Give the position of every Plasmodium parasite and every leukocyte.
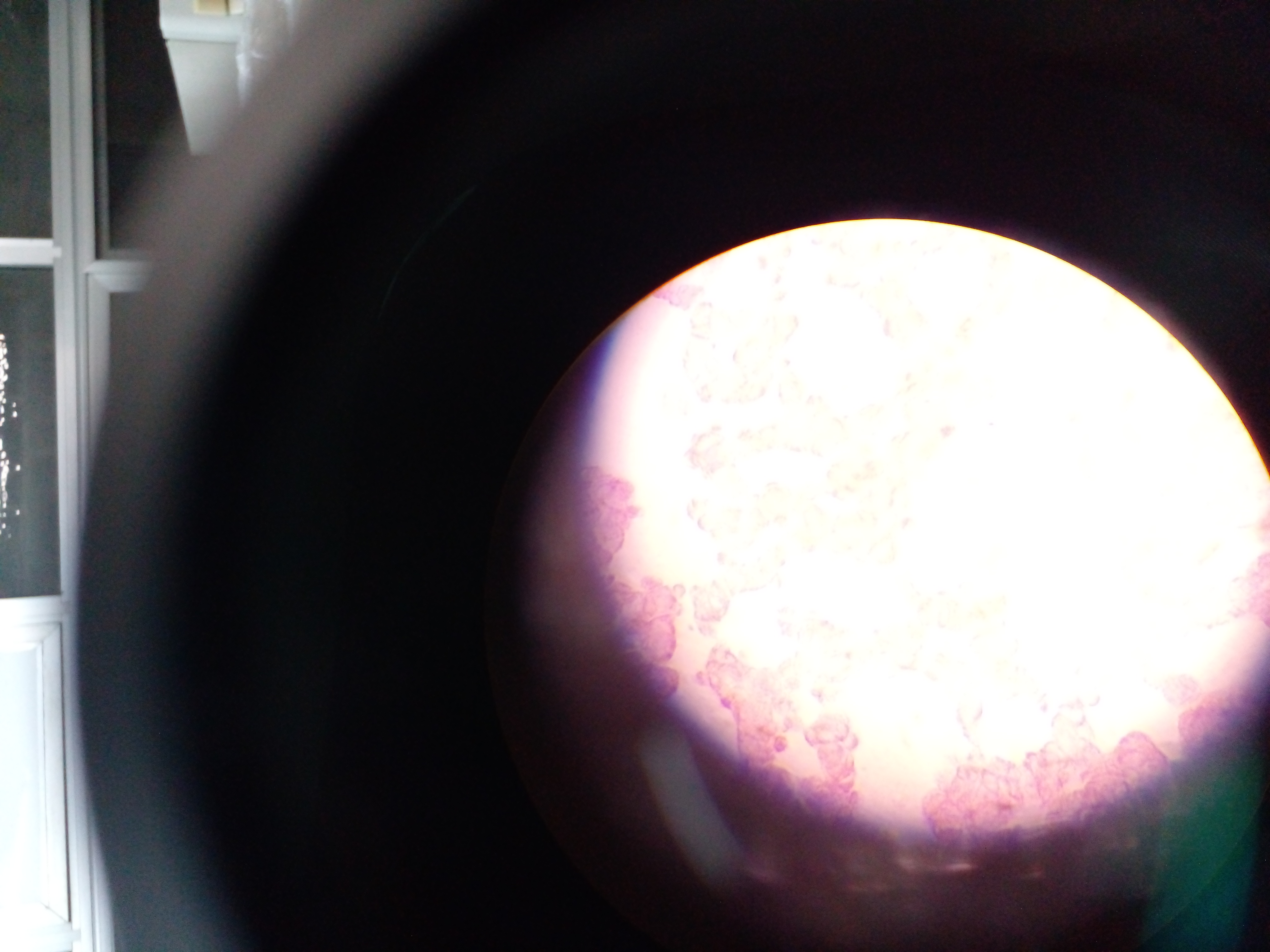

Approximate centers as {x, y} in pixels.
Plasmodium parasites: {214, 13}, {760, 263}, {776, 280}, {828, 282}, {707, 304}, {885, 328}, {695, 331}, {713, 347}, {734, 357}, {684, 363}, {787, 363}, {907, 380}, {762, 392}, {702, 394}, {780, 395}, {811, 399}, {840, 421}, {991, 423}, {716, 428}, {946, 432}, {743, 435}, {898, 437}, {794, 451}, {771, 486}, {834, 494}, {892, 497}, {690, 509}, {778, 519}, {906, 522}, {809, 547}, {719, 558}, {781, 563}, {1235, 580}, {942, 592}, {919, 608}, {826, 623}, {942, 626}, {1208, 628}, {782, 629}, {874, 632}, {846, 655}, {903, 667}, {1017, 668}, {932, 678}, {818, 695}, {1097, 701}, {724, 703}, {1041, 707}, {980, 714}, {1080, 721}, {961, 730}, {1029, 755}.
No leukocytes observed.

Mobile-phone photograph taken through the microscope. Thick blood smear. Sample from Ghana. Image is 1270×952 pixels. Single field of view.